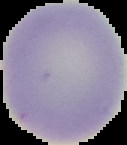
image size = 127×145 pixels
image type = segmented cell region on a black background
malaria status = uninfected
preparation = thin blood film